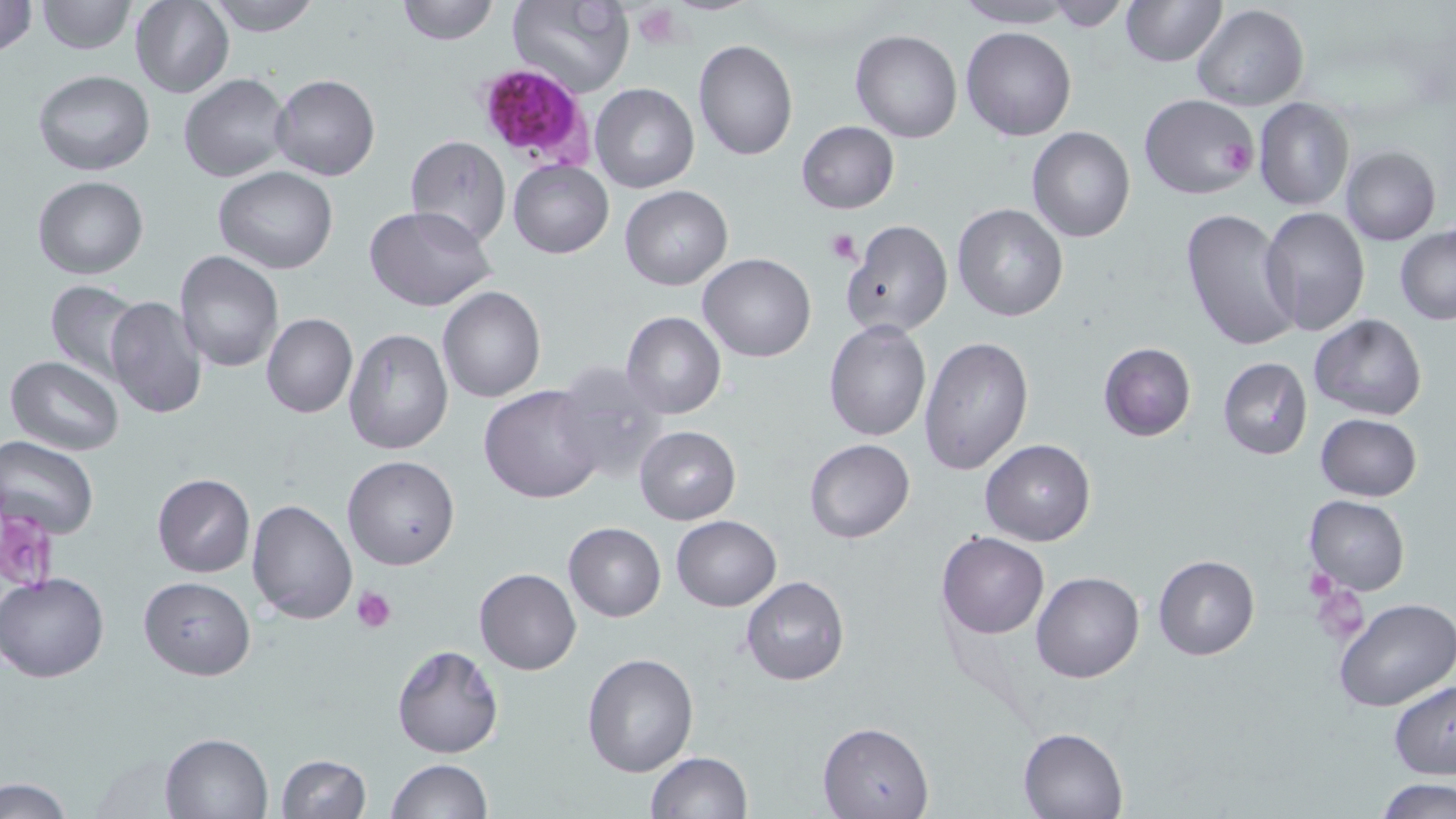
Summary:
  - Coordinate format: approximate bounding boxes as (x1, y1, x2, y2) in pixels
  - Plasmodium falciparum-infected red blood cell locations: (475, 64, 592, 168)
  - Platelet locations: (633, 6, 681, 44), (1216, 141, 1253, 174), (825, 227, 859, 265), (0, 501, 59, 594), (1303, 567, 1338, 602), (1310, 584, 1369, 644), (353, 586, 398, 634)
  - Uninfected red blood cell locations: (0, 0, 37, 59), (34, 0, 136, 55), (205, 0, 322, 37), (393, 0, 501, 45), (506, 0, 635, 98), (952, 0, 1079, 28), (1119, 0, 1227, 66), (131, 1, 233, 98), (1038, 1, 1135, 31), (1191, 4, 1308, 111), (960, 26, 1077, 141), (850, 30, 962, 143), (692, 38, 799, 162), (33, 70, 153, 175), (179, 74, 291, 182), (270, 74, 379, 181), (590, 83, 699, 194), (1138, 93, 1261, 201), (1253, 98, 1356, 212), (796, 121, 900, 215), (1026, 126, 1135, 243), (405, 136, 511, 247), (1340, 145, 1440, 246), (508, 158, 614, 259), (214, 167, 339, 274), (32, 176, 149, 279), (620, 185, 733, 291), (952, 203, 1069, 322), (365, 206, 496, 311), (1179, 206, 1302, 354), (1260, 207, 1370, 337), (841, 220, 953, 337), (1395, 224, 1456, 324), (173, 249, 283, 372), (699, 252, 816, 361), (45, 280, 144, 384), (437, 286, 546, 403), (104, 296, 208, 421), (620, 311, 727, 419), (261, 313, 358, 419), (1308, 314, 1429, 420), (824, 319, 932, 441), (342, 328, 454, 456), (918, 334, 1034, 475), (1098, 342, 1197, 441), (5, 356, 124, 455), (1217, 357, 1312, 462), (548, 362, 671, 485), (479, 384, 603, 504), (1315, 413, 1422, 502), (634, 426, 740, 525), (1, 437, 99, 541), (804, 438, 916, 544), (980, 439, 1096, 546), (342, 456, 460, 571), (152, 473, 255, 577), (1304, 495, 1410, 595), (247, 498, 357, 624), (671, 515, 781, 611), (563, 522, 666, 621), (937, 532, 1049, 638), (1153, 554, 1259, 659), (474, 567, 582, 675), (1031, 571, 1144, 683), (1, 572, 109, 682), (139, 577, 255, 679), (741, 577, 849, 687), (1333, 599, 1454, 714), (391, 643, 503, 758), (581, 651, 700, 778), (1389, 679, 1456, 781), (818, 722, 935, 818), (1018, 727, 1127, 818), (159, 732, 272, 818), (644, 751, 753, 818), (279, 754, 370, 818), (386, 759, 492, 817), (1377, 778, 1454, 819), (0, 780, 76, 818)
  - Slide-level diagnosis: Plasmodium falciparum
  - Preparation: thin blood film
  - Field of view: single
  - Magnification: 1000x
  - Modality: light microscopy
  - Image size: 1456×819 pixels
  - Stain: May-Grünwald-Giemsa